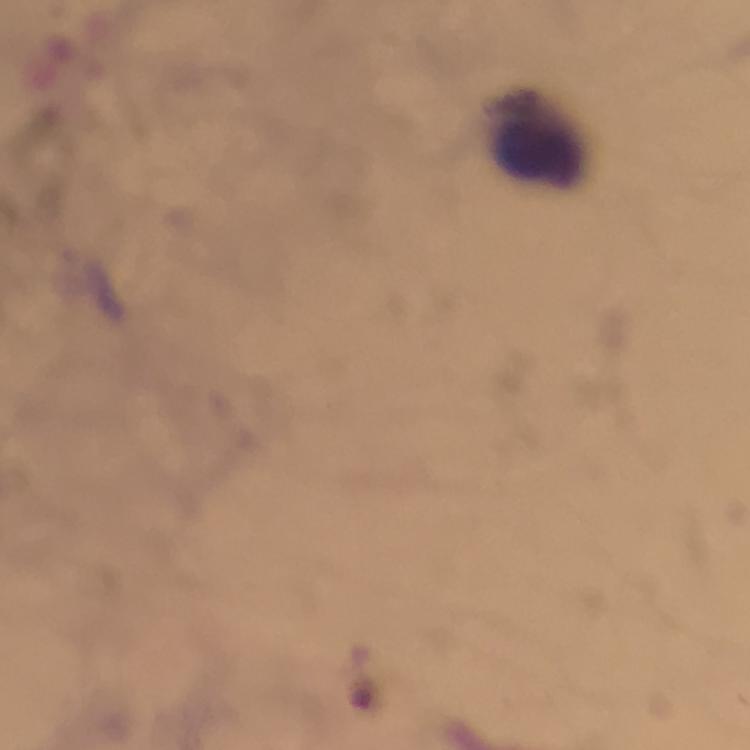

Approximate centers as [x, y] in pixels.
Summary:
  - Leukocyte locations: [537, 137]
  - Context: from a diagnostic examination for malaria
  - Immersion oil: applied
  - Stain: Giemsa
  - Capture: smartphone camera through the microscope
  - Preparation: thick blood film
  - Magnification: 100x
  - Cropped from: a single field of view
  - Image size: 750×750 pixels
  - Plasmodium parasites: none seen